State the blood parasite species.
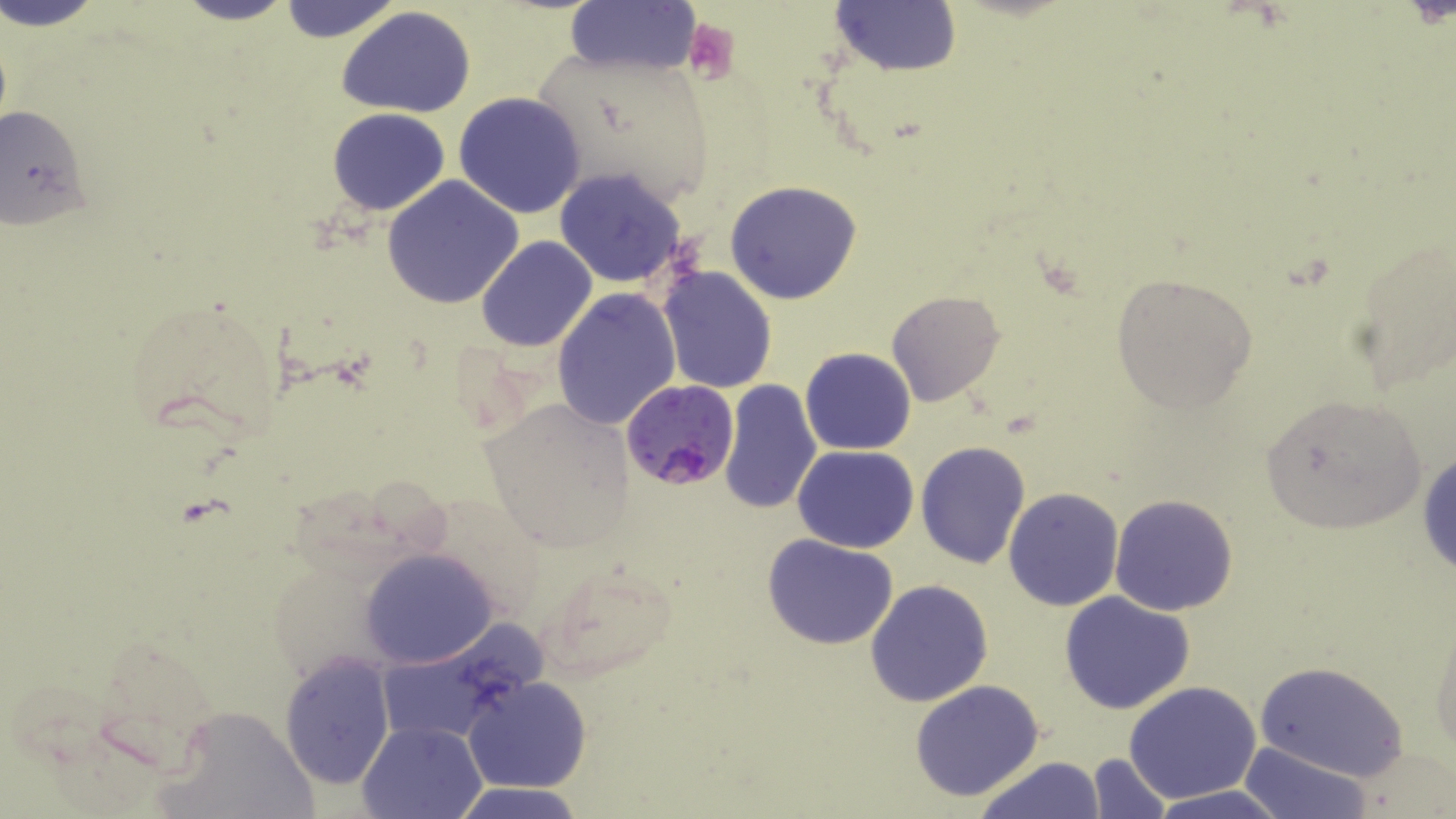

Plasmodium falciparum.

{
  "platelet_locations": "approximate bounding boxes as (x1, y1, x2, y2) in pixels: (682, 19, 741, 83)",
  "image_size": "1456×819 pixels",
  "uninfected_red_blood_cell_locations": "approximate bounding boxes as (x1, y1, x2, y2) in pixels: (2, 0, 106, 30), (169, 0, 300, 25), (276, 1, 403, 44), (829, 1, 962, 74), (562, 2, 702, 76), (337, 6, 478, 116), (540, 51, 707, 199), (453, 91, 587, 219), (0, 102, 91, 231), (327, 107, 449, 215), (553, 167, 690, 289), (382, 176, 524, 307), (725, 179, 863, 303), (1347, 232, 1455, 393), (476, 235, 597, 353), (658, 266, 778, 394), (1110, 272, 1260, 413), (551, 289, 680, 432), (886, 290, 1005, 408), (118, 296, 284, 441), (800, 348, 917, 455), (720, 379, 822, 517), (1256, 392, 1429, 536), (477, 395, 635, 553), (916, 442, 1032, 569), (793, 445, 918, 553), (1416, 446, 1456, 581), (1003, 488, 1124, 611), (1109, 494, 1239, 615), (761, 532, 900, 651), (359, 549, 497, 669), (541, 560, 678, 680), (865, 579, 994, 705), (1059, 591, 1197, 715), (1430, 614, 1456, 759), (280, 652, 394, 789), (1256, 662, 1408, 782), (463, 676, 592, 794), (908, 680, 1046, 803), (1122, 681, 1263, 804), (155, 702, 319, 819), (359, 719, 486, 818), (1240, 740, 1371, 819), (1087, 753, 1174, 819), (977, 756, 1105, 819), (453, 784, 585, 819), (1145, 786, 1291, 819)",
  "stain": "May-Grünwald-Giemsa",
  "modality": "light microscopy",
  "magnification": "1000x",
  "field_of_view": "single",
  "plasmodium_falciparum_infected_red_blood_cell_locations": "approximate bounding boxes as (x1, y1, x2, y2) in pixels: (624, 380, 742, 489)",
  "preparation": "thin blood smear"
}